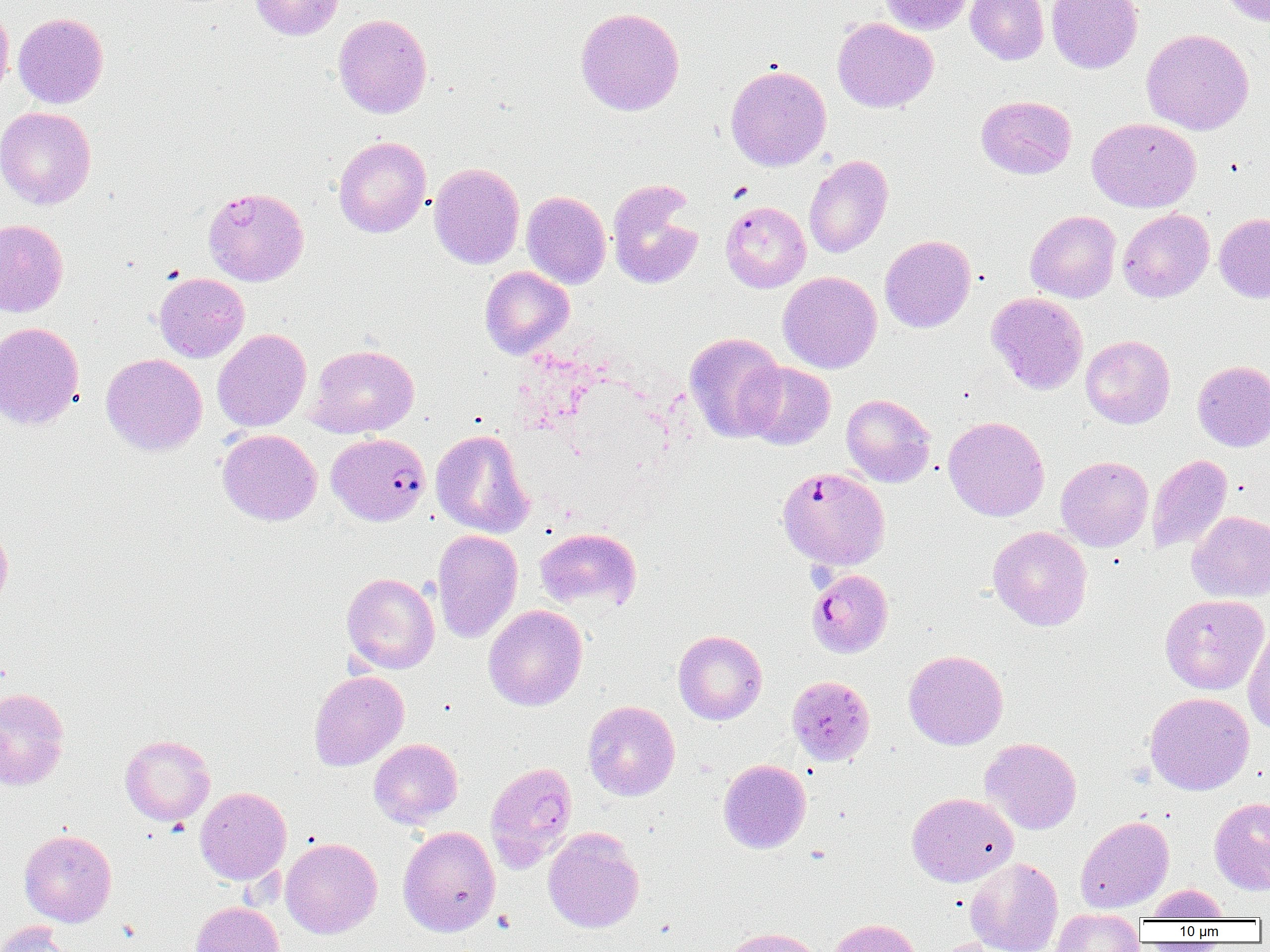

Approximate bounding boxes as (x1, y1, x2, y2) in pixels. Uninfected red blood cell locations: (250, 0, 343, 40), (880, 0, 975, 35), (965, 0, 1049, 65), (1046, 0, 1142, 73), (1216, 0, 1270, 26), (0, 5, 14, 103), (575, 7, 685, 116), (12, 13, 108, 108), (333, 14, 432, 118), (832, 18, 938, 112), (1141, 28, 1254, 135), (725, 64, 831, 171), (976, 95, 1077, 179), (0, 106, 96, 209), (1087, 117, 1200, 212), (333, 136, 431, 238), (804, 155, 893, 258), (429, 162, 525, 269), (606, 180, 704, 290), (521, 190, 611, 288), (1117, 208, 1214, 302), (1025, 210, 1121, 303), (1214, 213, 1270, 303), (0, 219, 69, 317), (880, 235, 976, 332), (480, 266, 574, 359), (778, 271, 881, 373), (154, 273, 249, 363), (987, 292, 1088, 395), (0, 322, 85, 429), (212, 329, 311, 432), (685, 332, 786, 442), (1080, 335, 1175, 428), (307, 344, 419, 438), (100, 353, 207, 456), (1192, 360, 1270, 452), (742, 362, 835, 450), (841, 394, 936, 487), (943, 416, 1050, 521), (217, 429, 322, 525), (431, 429, 533, 537), (1147, 454, 1232, 554), (1056, 455, 1154, 551), (1188, 511, 1270, 602), (0, 520, 12, 613), (988, 526, 1092, 631), (534, 527, 642, 612), (432, 529, 523, 643), (342, 573, 439, 674), (1160, 594, 1269, 695), (484, 605, 587, 711), (1243, 624, 1270, 734), (673, 630, 767, 724), (903, 649, 1008, 750), (309, 670, 409, 771), (0, 687, 70, 790), (1145, 692, 1254, 795), (583, 700, 680, 800), (120, 735, 215, 825), (980, 737, 1082, 835), (369, 738, 463, 828), (718, 759, 811, 853), (195, 786, 292, 884), (907, 792, 1018, 886), (1209, 796, 1270, 895), (1076, 815, 1173, 913), (398, 825, 500, 937), (19, 829, 117, 927), (543, 829, 644, 933), (280, 837, 382, 938), (965, 857, 1063, 952), (1146, 884, 1229, 920), (191, 901, 285, 952), (1052, 909, 1145, 952), (827, 918, 922, 952), (0, 921, 77, 952), (722, 927, 826, 952), (933, 938, 1018, 952). Plasmodium falciparum-infected red blood cell locations: (204, 186, 309, 286), (720, 201, 811, 293), (327, 432, 430, 526), (777, 467, 891, 570), (806, 568, 892, 657), (787, 675, 874, 766), (485, 762, 578, 872). Slide-level diagnosis: Plasmodium falciparum. Thin blood smear. 1000x magnification. Image is 1270×952 pixels. Optical microscopy. Single field of view.